Outline each Plasmodium falciparum-infected red blood cell.
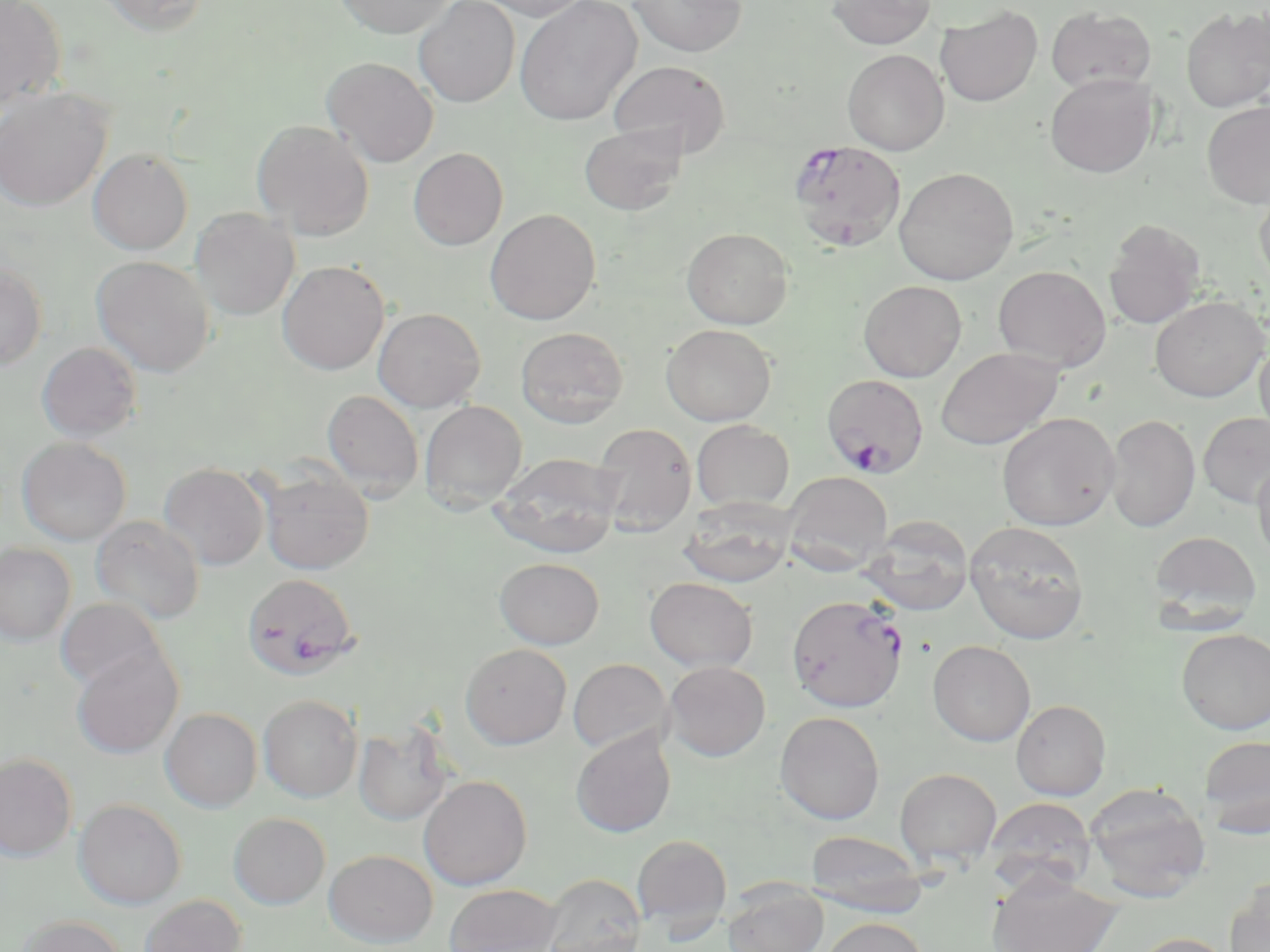

Approximate bounding boxes as [x1, y1, x2, y2] in pixels.
Plasmodium falciparum-infected red blood cells: [788, 139, 906, 251], [822, 373, 929, 476], [242, 572, 360, 682], [786, 594, 908, 713].

slide-level diagnosis = Plasmodium falciparum
field of view = one of a larger specimen
magnification = 1000x
modality = light microscopy
preparation = thin blood film
stain = May-Grünwald-Giemsa
image size = 1270×952 pixels
uninfected red blood cell locations = approximate bounding boxes as [x1, y1, x2, y2] in pixels: [0, 0, 67, 112], [93, 0, 211, 34], [334, 0, 453, 38], [413, 0, 520, 107], [476, 0, 592, 21], [628, 0, 747, 57], [826, 0, 936, 49], [515, 1, 642, 125], [935, 5, 1043, 107], [1046, 6, 1156, 93], [1181, 6, 1270, 112], [842, 49, 949, 155], [322, 57, 439, 167], [609, 60, 730, 158], [1045, 73, 1157, 177], [0, 87, 113, 212], [1202, 101, 1270, 209], [251, 119, 375, 240], [578, 123, 687, 216], [408, 147, 508, 250], [88, 148, 194, 255], [893, 167, 1018, 285], [1254, 182, 1270, 291], [190, 207, 299, 320], [484, 208, 601, 325], [1103, 219, 1206, 329], [682, 227, 793, 329], [92, 255, 215, 377], [277, 260, 390, 374], [0, 262, 48, 370], [993, 265, 1111, 371], [858, 280, 966, 382], [1150, 296, 1267, 402], [372, 307, 486, 412], [661, 324, 776, 426], [516, 327, 628, 428], [1255, 339, 1270, 443], [36, 341, 142, 441], [935, 347, 1063, 451], [322, 390, 424, 499], [419, 400, 527, 511], [1198, 412, 1270, 509], [997, 413, 1119, 531], [1105, 413, 1200, 532], [692, 420, 794, 511], [591, 422, 697, 536], [16, 437, 132, 546], [492, 452, 623, 558], [1252, 456, 1270, 567], [159, 463, 270, 570], [257, 464, 374, 575], [781, 471, 893, 575], [679, 499, 797, 587], [91, 515, 204, 624], [863, 515, 974, 615], [964, 520, 1090, 645], [1149, 531, 1261, 627], [0, 542, 76, 646], [494, 557, 604, 649], [644, 576, 757, 672], [55, 598, 168, 692], [1177, 628, 1270, 734], [927, 640, 1035, 746], [460, 643, 572, 749], [71, 646, 184, 759], [567, 658, 672, 754], [663, 661, 770, 761], [258, 694, 362, 802], [1011, 699, 1110, 800], [160, 707, 262, 812], [775, 711, 885, 825], [353, 720, 454, 826], [570, 728, 676, 838], [1199, 734, 1270, 838], [0, 753, 77, 861], [895, 768, 1002, 869], [418, 775, 533, 890], [1084, 782, 1210, 903], [984, 796, 1096, 896], [73, 799, 186, 909], [228, 812, 331, 909], [807, 829, 927, 916], [632, 834, 732, 933], [324, 849, 438, 947], [987, 872, 1121, 952], [542, 873, 646, 952], [1225, 878, 1270, 952], [723, 882, 828, 952], [444, 883, 562, 952], [138, 894, 247, 952], [17, 915, 128, 952], [820, 917, 928, 952], [1129, 932, 1235, 952]